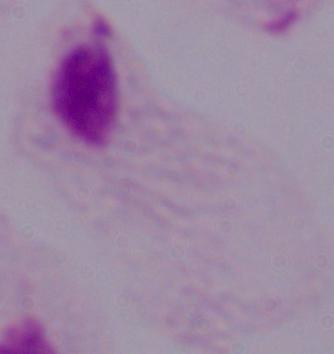

magnification: 1000x
modality: micrograph
identification: trichomonad